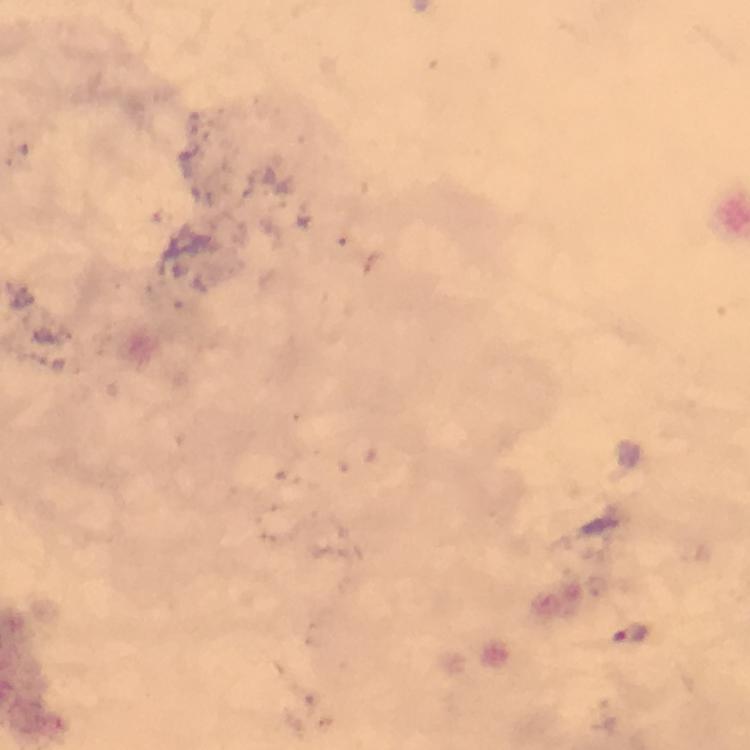

Approximate object centers, in pixels from the top-left corner.
Summary:
  - Malaria parasite locations: (x=631, y=636)
  - Stain: Giemsa
  - Immersion oil: used
  - Cropped from: a single field of view
  - Magnification: 100x
  - Capture: smartphone camera through the microscope
  - Image size: 750×750 pixels
  - Context: from a malaria diagnostic workup
  - Preparation: thick blood film